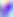 Toxoplasma gondii is seen. Micrograph. 400x magnification.